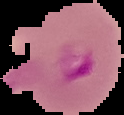
Image is 124×115 pixels. Result: malaria parasites detected. From a thin blood film. Segmented cell region on a black background.